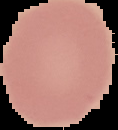
image type = segmented cell region on a black background
result = negative for Plasmodium parasites
preparation = thin blood film
image size = 118×130 pixels